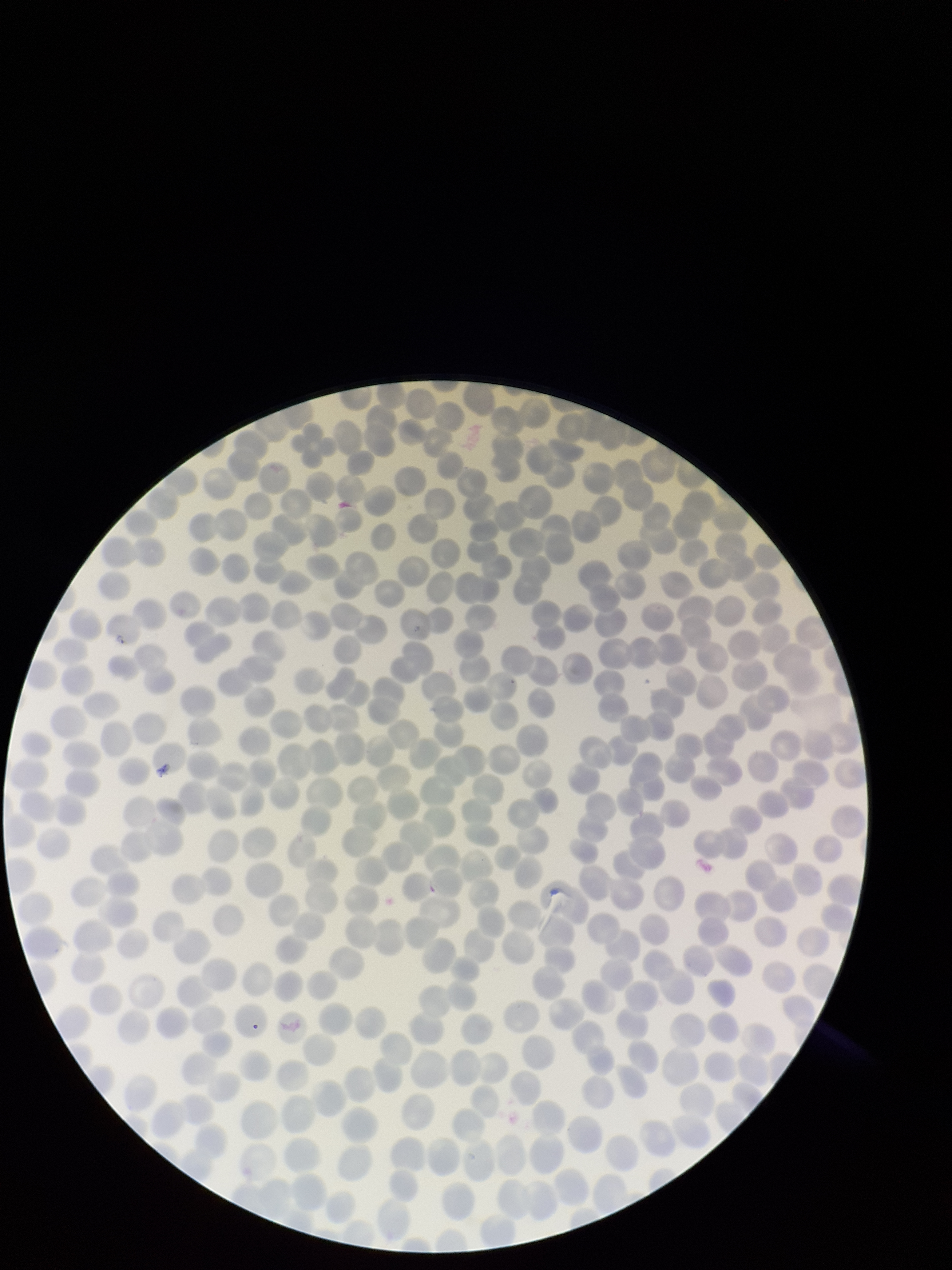

Parasitized red blood cell count: 1. Image is 952×1270 pixels. Species reported for this patient: Plasmodium falciparum. Single field of view. Red blood cell count: 273. Patient malaria status: infected. Parasitized red blood cells: identified. Giemsa stain. Preparation: thin. Smartphone photograph taken through the eyepiece of a microscope.